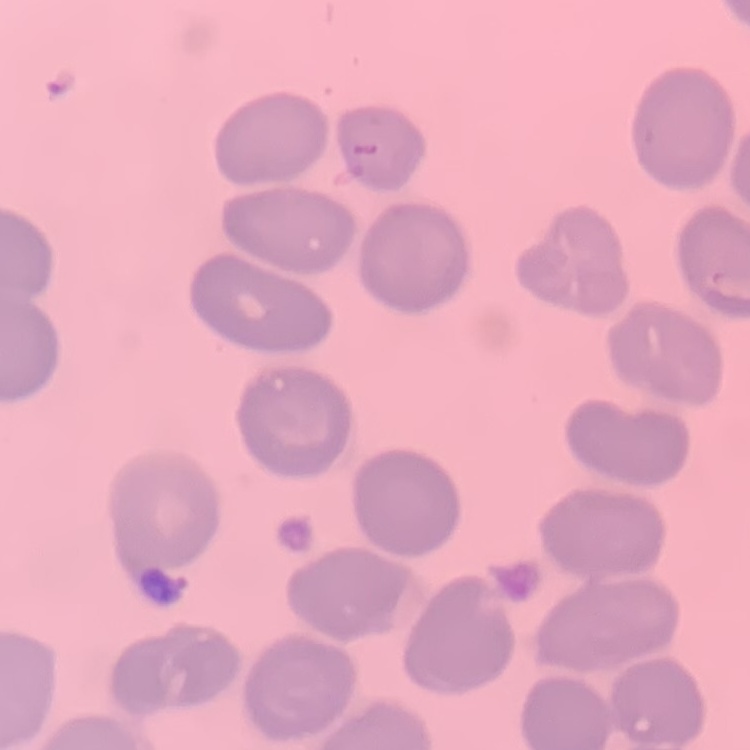

Summary:
  - Red blood cell morphology: no rouleaux formation
  - Preparation: thin blood film
  - Image type: one tile cut from a larger photomicrograph
  - Stain: Field's or Giemsa